Report the malaria status of this cell.
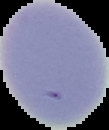
It is uninfected.

Image is 109×130 pixels. Segmented cell region on a black background. From a thin blood smear.